Give the extent of all Plasmodium malariae-infected red blood cells.
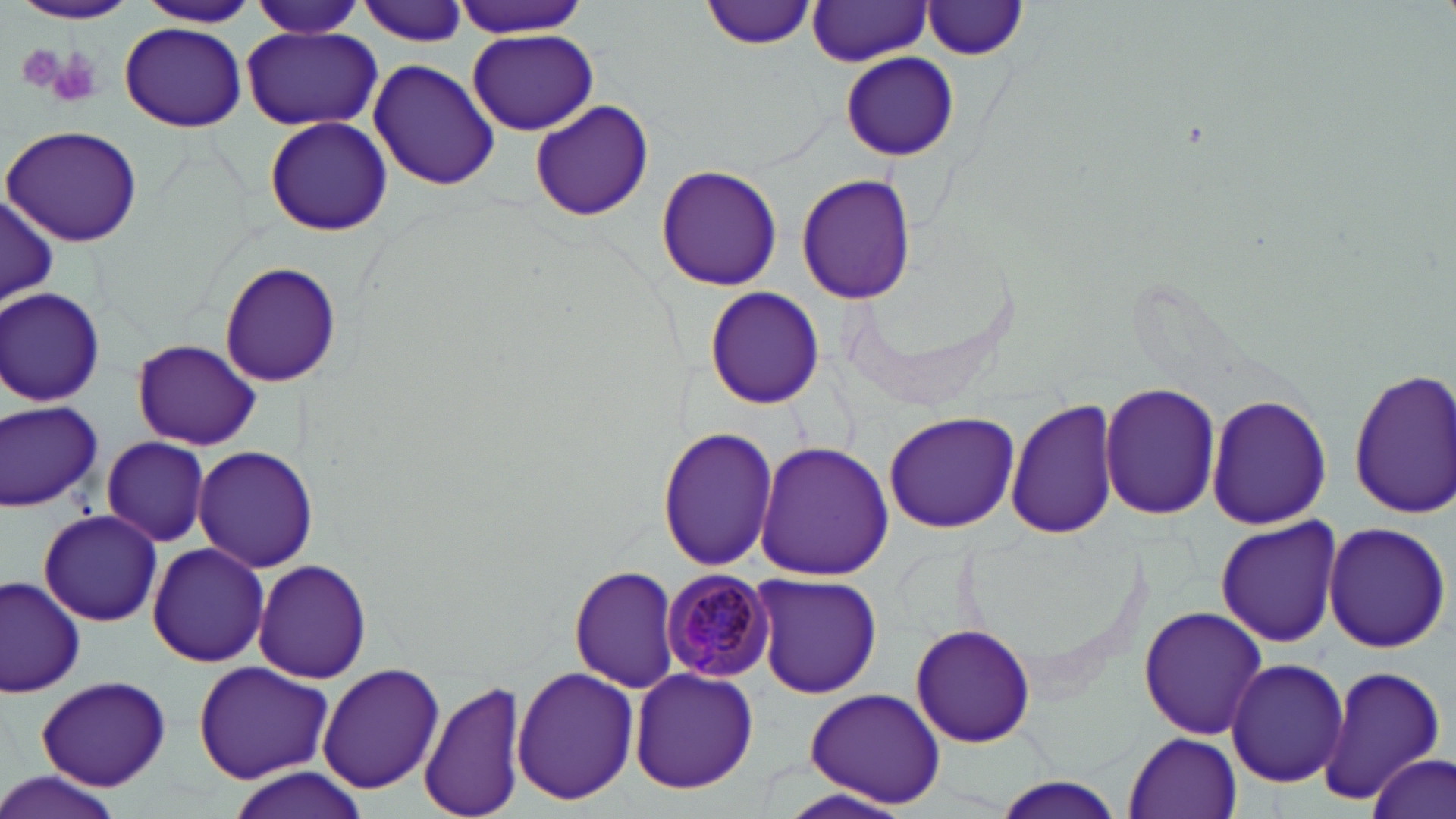
Approximate bounding boxes as [x1, y1, x2, y2] in pixels.
Plasmodium malariae-infected red blood cells: [662, 569, 776, 681].

Uninfected red blood cell locations: [8, 0, 140, 25], [353, 0, 469, 49], [453, 0, 589, 38], [705, 0, 816, 50], [134, 1, 259, 29], [248, 1, 366, 37], [808, 2, 935, 66], [921, 2, 1031, 62], [119, 23, 247, 131], [243, 26, 380, 131], [467, 28, 597, 136], [842, 52, 958, 162], [368, 58, 500, 190], [529, 100, 655, 221], [264, 116, 391, 237], [2, 126, 146, 246], [655, 166, 782, 290], [795, 173, 918, 303], [1, 191, 58, 308], [219, 261, 342, 389], [703, 285, 826, 410], [1, 287, 106, 406], [133, 339, 259, 450], [1348, 368, 1456, 519], [1099, 382, 1221, 521], [1205, 392, 1331, 531], [1006, 397, 1123, 542], [0, 398, 103, 513], [883, 412, 1021, 534], [658, 425, 777, 573], [100, 436, 213, 547], [756, 441, 892, 581], [194, 446, 319, 573], [39, 507, 161, 627], [1215, 517, 1344, 649], [1322, 522, 1452, 653], [148, 541, 268, 667], [254, 560, 374, 684], [568, 564, 682, 693], [749, 573, 883, 699], [1, 575, 86, 697], [1138, 606, 1267, 739], [911, 623, 1037, 748], [1226, 658, 1349, 788], [192, 661, 335, 787], [317, 662, 444, 795], [1314, 665, 1451, 800], [512, 667, 639, 804], [629, 669, 758, 794], [34, 675, 173, 790], [419, 677, 527, 819], [802, 687, 949, 810], [1124, 732, 1242, 817], [1369, 755, 1453, 818], [226, 767, 370, 819], [0, 776, 129, 819], [991, 777, 1130, 817], [774, 787, 921, 819]. Platelet locations: [13, 40, 71, 96], [38, 45, 103, 108]. Slide-level diagnosis: Plasmodium malariae. Image is 1456×819 pixels. One field of a larger specimen. Light microscopy. Thin blood smear. May-Grünwald-Giemsa stain. Captured at 1000x magnification.